Comment on the morphology of the erythrocytes.
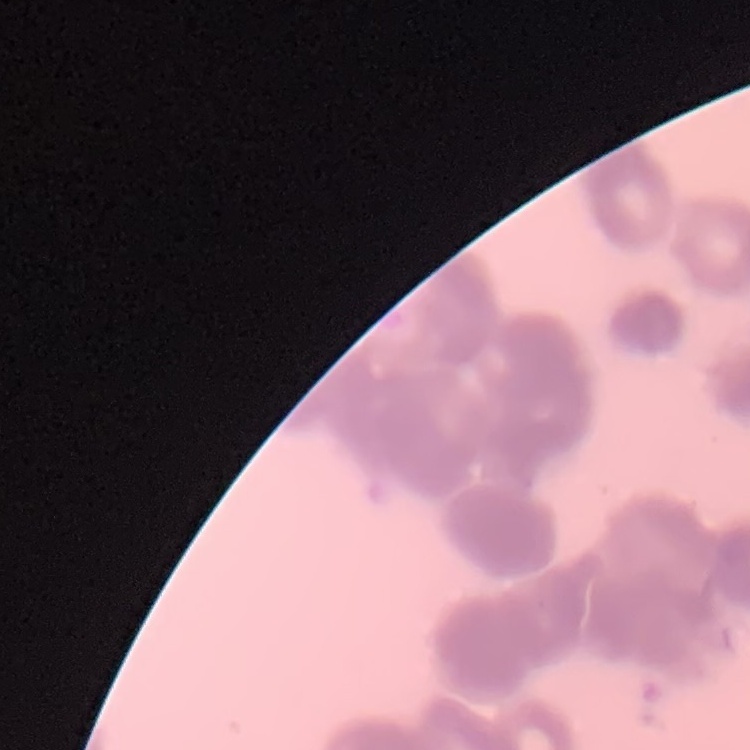

Rouleaux formation.

One tile cut from a larger photomicrograph. Thin blood smear. Field's or Giemsa stain.